Report the malaria status of this cell.
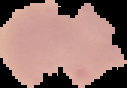
Parasitized.

{
  "image_size": "127×88 pixels",
  "preparation": "thin blood film",
  "image_type": "segmented cell region on a black background"
}